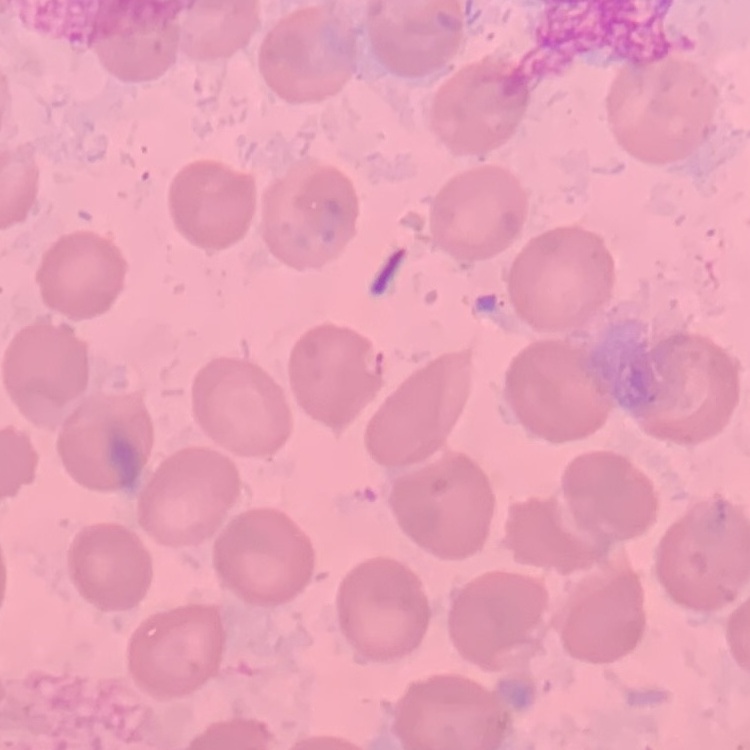
Summary:
  - Erythrocyte morphology: no rouleaux formation
  - Stain: Field's or Giemsa
  - Preparation: thin peripheral smear
  - Image type: square crop of a larger photomicrograph